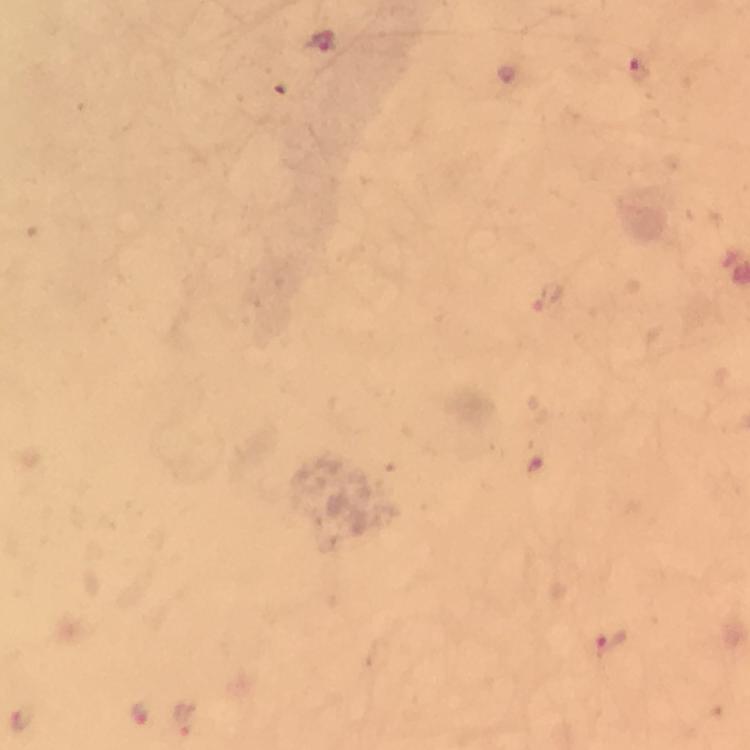

context = from a diagnostic examination for malaria
image size = 750×750 pixels
preparation = thick smear
capture = smartphone mounted on the microscope
Plasmodium parasite locations = approximate centers as [x, y] in pixels: [323, 42], [638, 68], [545, 294], [610, 646], [139, 712], [21, 718], [184, 718]
immersion oil = applied
cropped from = a single field of view
magnification = 100x
stain = Giemsa